Locate and identify every blood parasite.
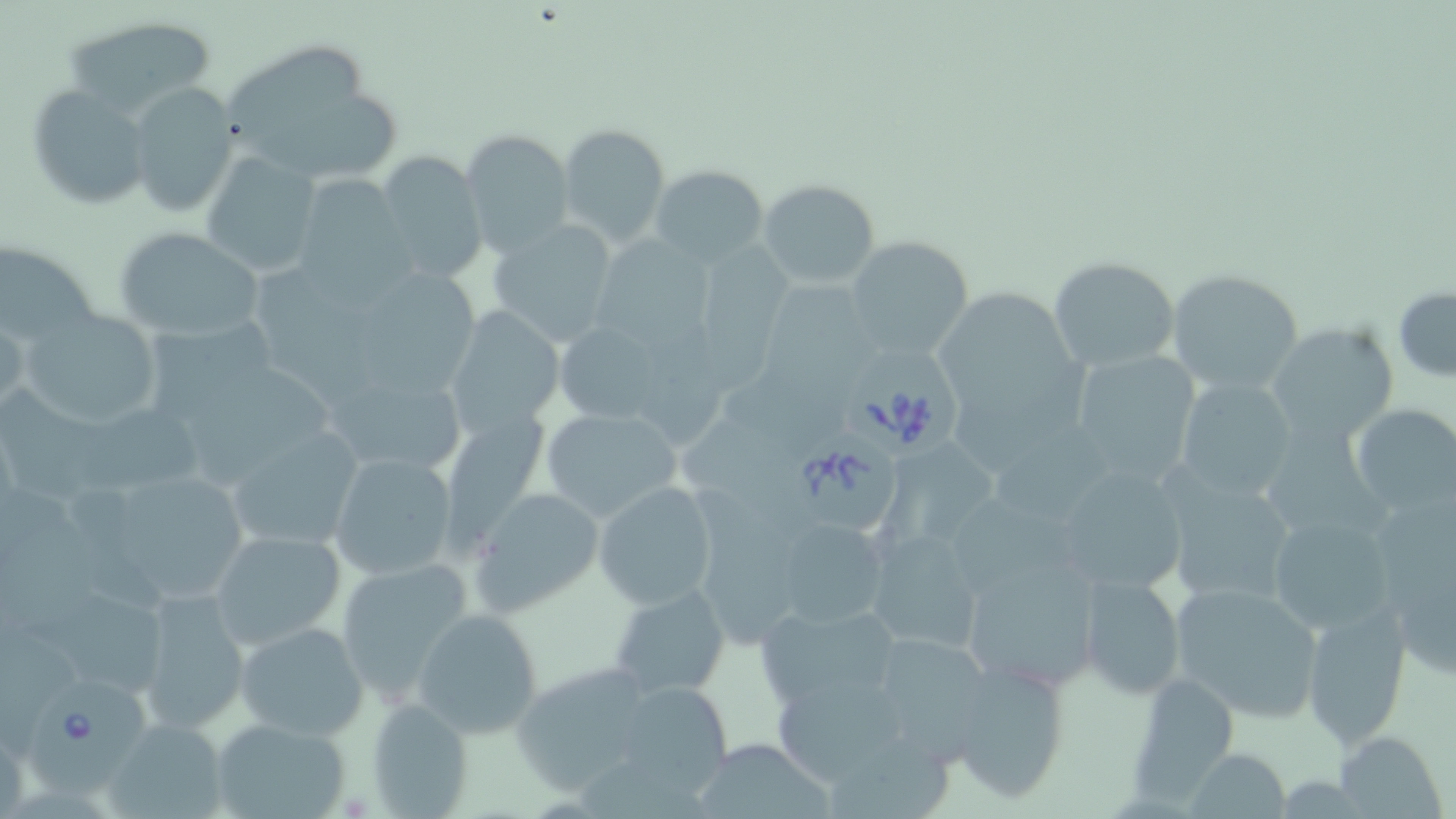
Approximate bounding boxes as (x1,y1)-(x2,y2) corner pairs in pixels.
Babesia divergens-infected red blood cells: (840,341)-(970,462), (775,421)-(905,536), (29,675)-(153,797).
No Plasmodium falciparum, Plasmodium ovale, Plasmodium malariae, Plasmodium vivax, or Trypanosoma brucei observed.

slide-level diagnosis = Babesia divergens
field of view = one of a larger specimen
magnification = 1000x
modality = optical microscopy
stain = May-Grünwald-Giemsa
image size = 1456×819 pixels
uninfected red blood cell locations = approximate bounding boxes as (x1,y1)-(x2,y2) corner pairs in pixels: (59,14)-(218,123), (215,42)-(371,149), (127,82)-(239,216), (29,86)-(152,210), (254,96)-(404,178), (557,123)-(671,249), (460,128)-(574,257), (374,151)-(489,285), (200,154)-(322,276), (651,165)-(770,267), (296,174)-(407,288), (758,178)-(879,288), (486,218)-(623,345), (114,229)-(264,340), (694,230)-(803,396), (844,235)-(977,361), (602,237)-(718,351), (0,242)-(103,348), (1048,255)-(1179,373), (258,257)-(392,419), (733,263)-(875,448), (1164,269)-(1308,397), (359,271)-(484,391), (941,279)-(1078,423), (1393,287)-(1456,382), (444,305)-(563,436), (141,308)-(278,431), (21,309)-(167,433), (0,314)-(28,417), (639,316)-(739,458), (553,319)-(670,427), (1267,321)-(1400,448), (1068,349)-(1201,485), (336,362)-(470,477), (194,366)-(338,489), (961,370)-(1092,481), (1175,377)-(1298,502), (5,380)-(218,510), (1348,402)-(1456,515), (538,407)-(681,525), (681,407)-(807,526), (223,426)-(365,553), (1270,426)-(1396,551), (874,441)-(1011,551), (1000,448)-(1126,532), (326,449)-(460,583), (1049,461)-(1193,596), (1158,471)-(1299,610), (689,473)-(806,645), (123,475)-(264,601), (593,482)-(718,609), (1,483)-(107,626), (1366,484)-(1456,667), (472,488)-(604,616), (955,496)-(1093,601), (1265,513)-(1399,638), (770,517)-(888,629), (864,527)-(984,655), (209,529)-(345,650), (961,551)-(1102,695), (334,557)-(476,699), (1079,573)-(1185,700), (1167,580)-(1326,723), (611,583)-(730,699), (138,589)-(250,733), (29,590)-(172,697), (753,601)-(901,710), (1300,603)-(1413,746), (412,608)-(544,739), (234,620)-(369,741), (864,630)-(999,761), (946,657)-(1073,804), (510,661)-(664,793), (1125,673)-(1242,800), (637,679)-(735,798), (624,684)-(733,798), (774,685)-(905,783), (366,698)-(476,816), (103,717)-(230,818), (209,717)-(353,819), (1333,729)-(1448,819), (693,732)-(834,819), (829,735)-(951,818), (1184,747)-(1291,819)
preparation = thin blood film